Identify the cell.
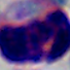

A leukocyte.

modality = micrograph
magnification = 1000x